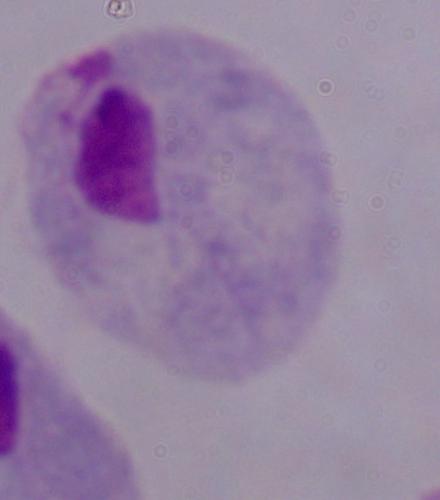

modality = micrograph
magnification = 1000x
identification = trichomonad